Assess the morphology of the red blood cells.
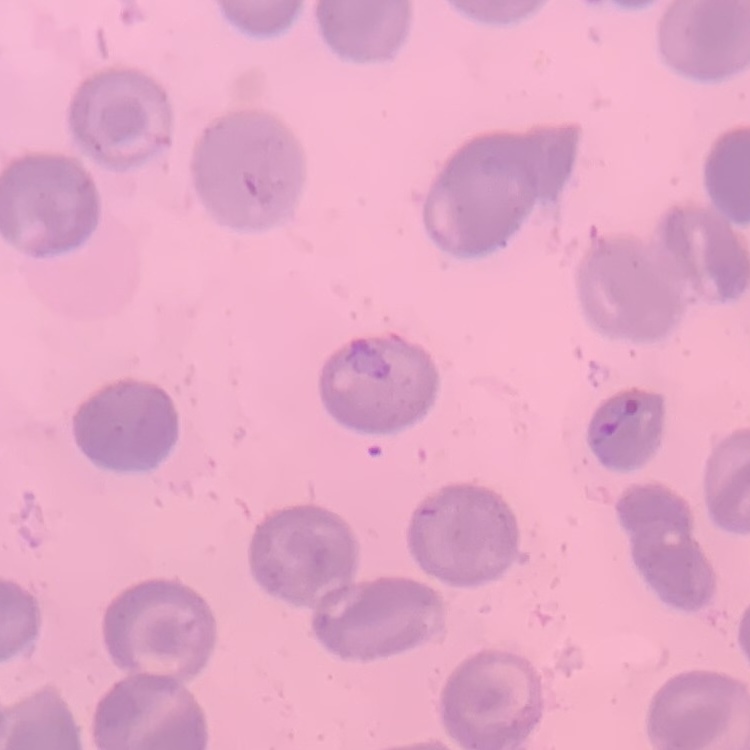

They show no rouleaux formation.

{
  "image_type": "square crop of a larger photomicrograph",
  "preparation": "thin blood film",
  "stain": "Field's or Giemsa"
}